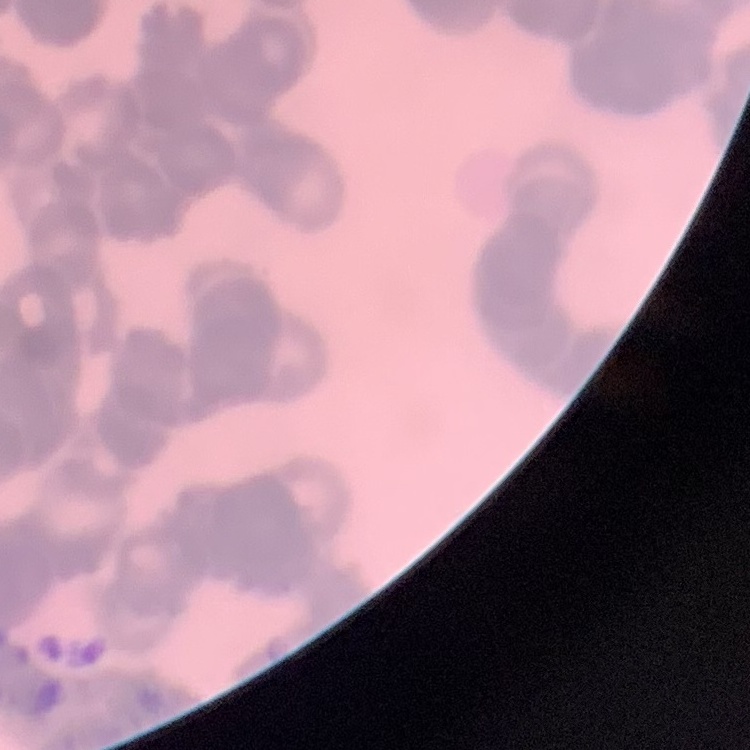
The erythrocytes show rouleaux formation. Square crop of a larger photomicrograph. Thin blood film. Field's or Giemsa stain.